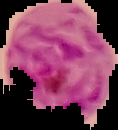
{
  "preparation": "thin blood film",
  "image_type": "segmented cell region on a black background",
  "result": "Plasmodium parasites identified",
  "image_size": "118×130 pixels"
}